Identify the parasite.
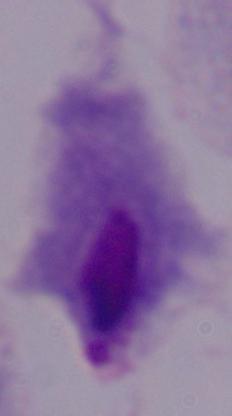
A trichomonad.

magnification = 1000x
modality = photomicrograph